Comment on the morphology of the erythrocytes.
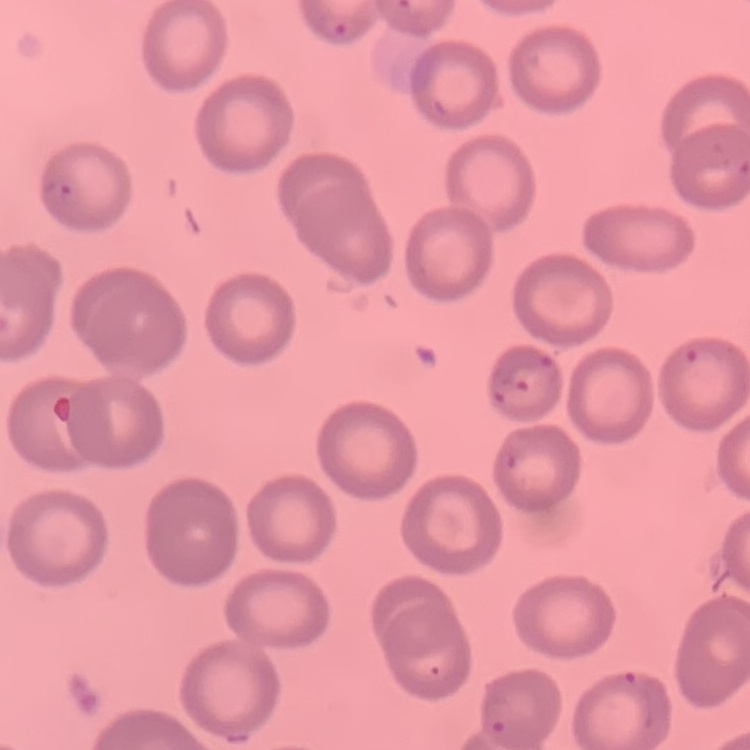
They show no rouleaux formation.

stain = Field's or Giemsa
image type = one tile cut from a larger photomicrograph
preparation = thin blood film